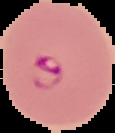

image_type: segmented cell region on a black background
preparation: thin blood smear
result: Plasmodium parasites detected
image_size: 115×133 pixels